Give the position of every malaria parasite.
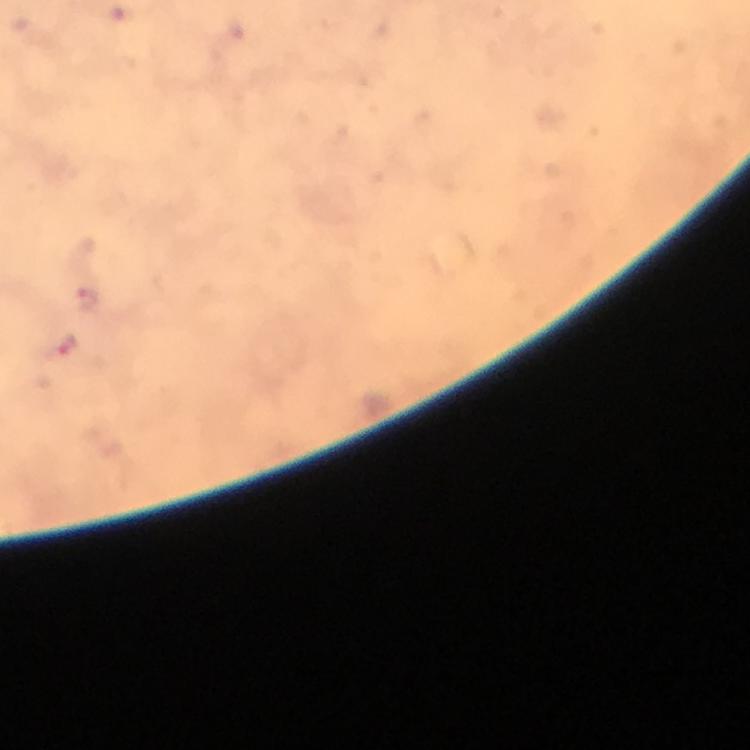

Approximate centers as (x, y) in pixels.
Malaria parasites: (86, 300), (61, 348).

Summary:
  - Stain: Giemsa
  - Magnification: 100x
  - Context: from a diagnostic examination for malaria
  - Preparation: thick blood film
  - Capture: smartphone camera through the microscope
  - Cropped from: one field of view
  - Image size: 750×750 pixels
  - Immersion oil: applied